Point out each leukocyte.
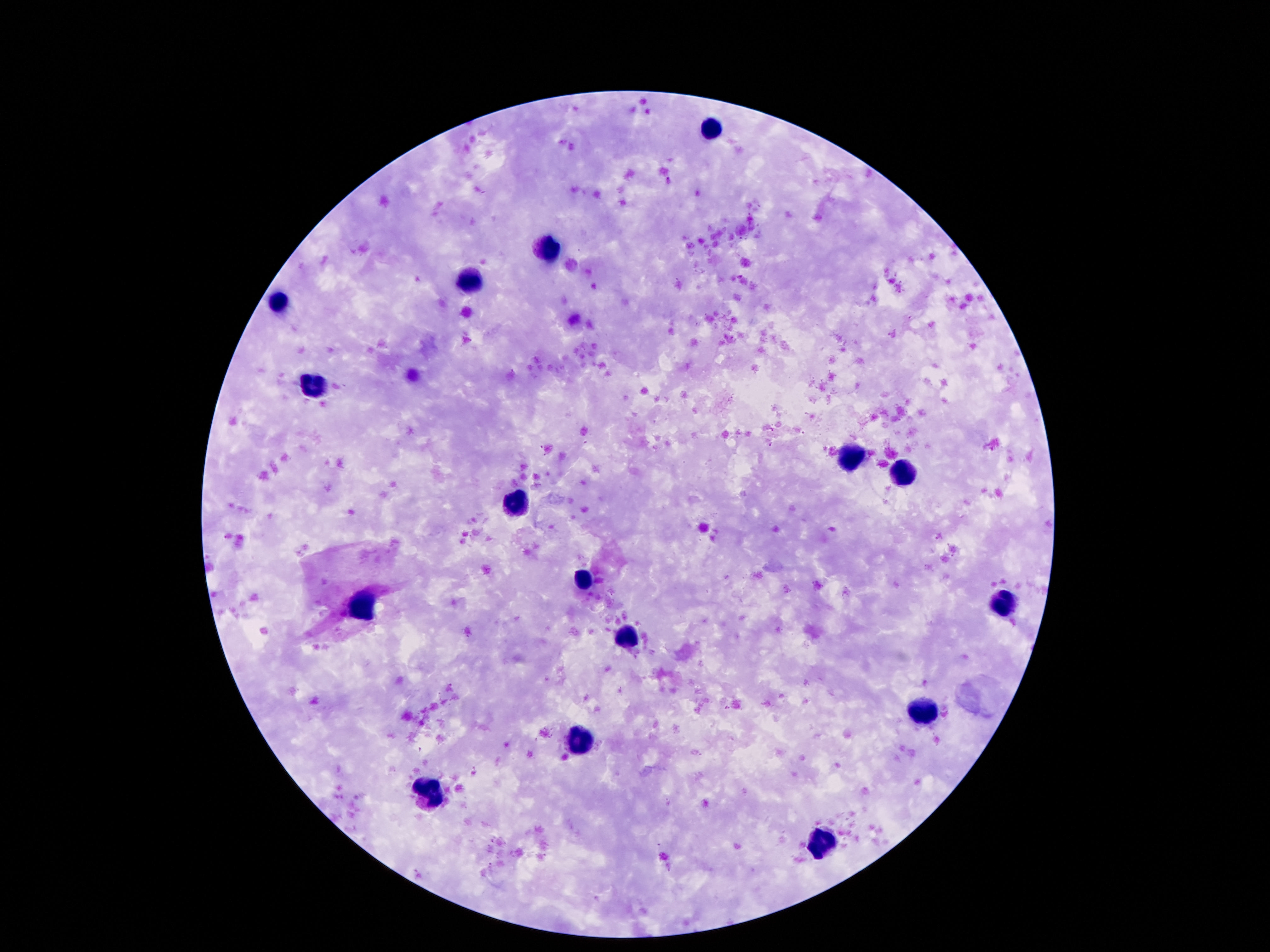

Approximate centers as (x, y) in pixels.
Leukocytes: (713, 128), (550, 246), (472, 278), (279, 305), (312, 387), (850, 458), (904, 475), (515, 504), (580, 579), (1000, 603), (360, 609), (626, 636), (922, 713), (578, 740), (433, 791), (820, 842).

Summary:
  - Magnification: 100x
  - Capture: smartphone camera through the microscope eyepiece
  - Field of view: one from this slide
  - Image size: 1270×952 pixels
  - Preparation: thick peripheral-blood smear
  - Patient malaria status: not infected
  - Stain: Giemsa